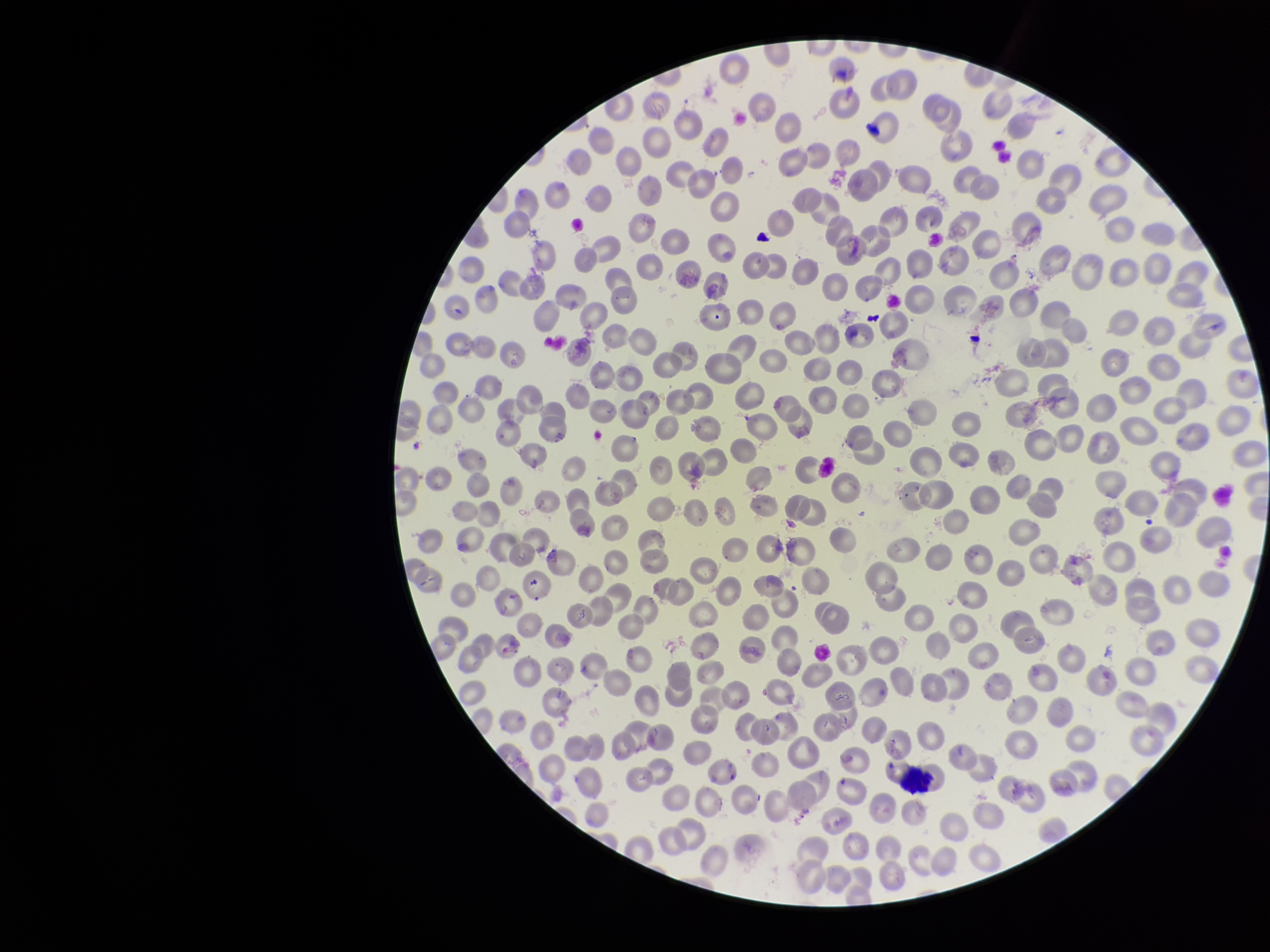
stain = Giemsa
image size = 1270×952 pixels
parasitized red blood cell count = 0
preparation = thin blood smear
capture = smartphone photograph through the microscope eyepiece
parasitized red blood cells = none detected
red blood cell count = 237
field of view = one from this slide
patient malaria status = negative